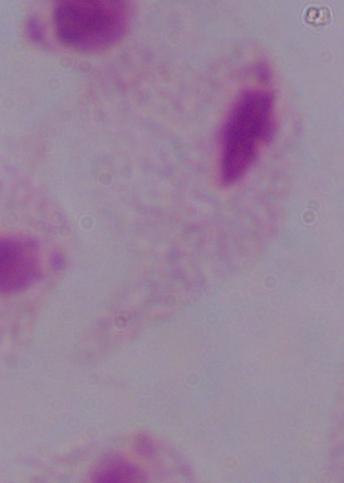 A trichomonad is seen. Captured at 1000x magnification. Photomicrograph.